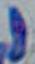

Summary:
  - Magnification: 1000x
  - Modality: photomicrograph
  - Identification: Toxoplasma gondii